Point out each leukocyte.
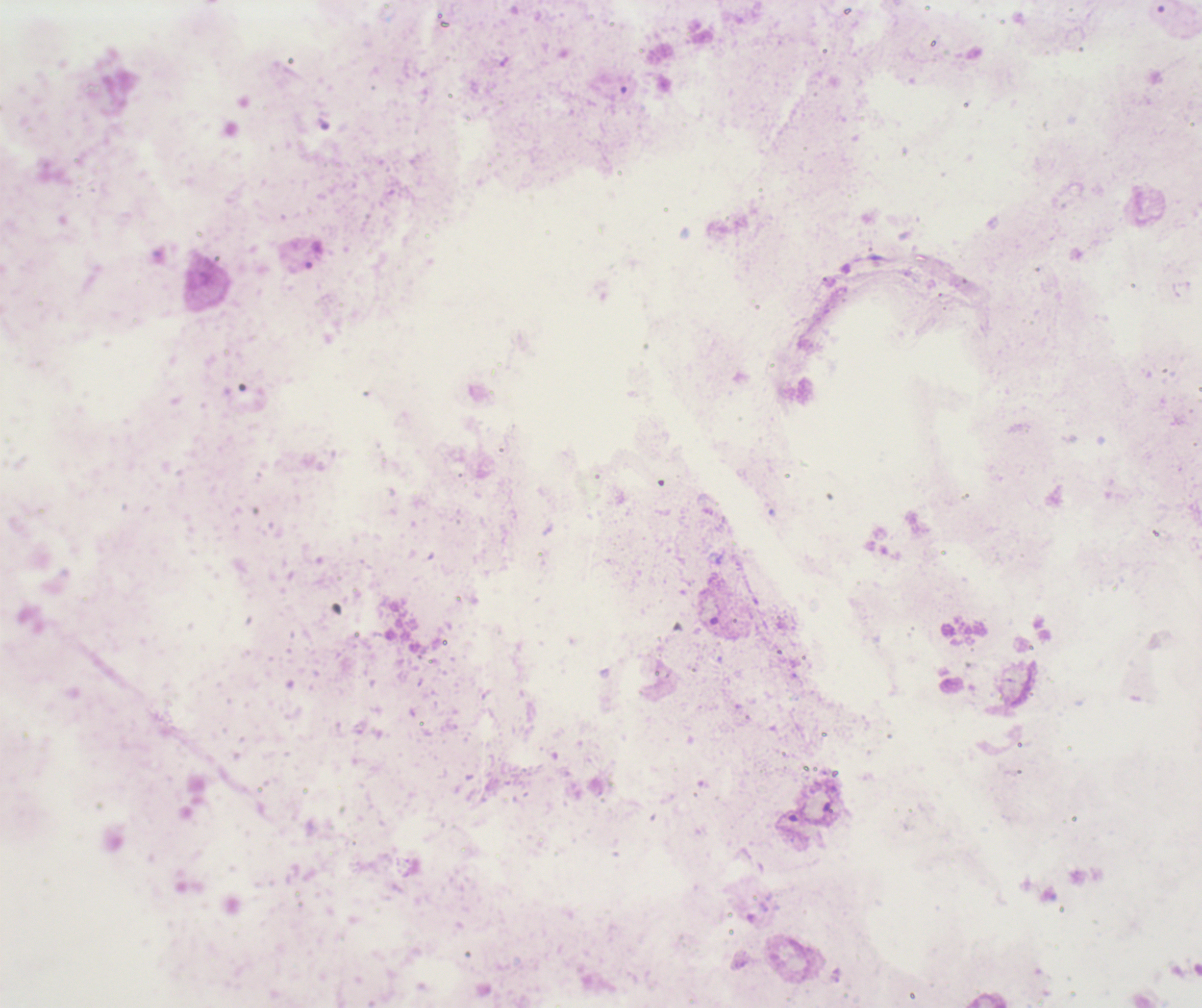

No leukocytes visible.

Result: no Plasmodium parasites detected. Coloration quality: bad. Thick blood film. Background quality: unsatisfactory. Romanowsky-stained preparation. 100x magnification. Previously used in an actual diagnosis. Image is 1202×1008 pixels. Single field of view.